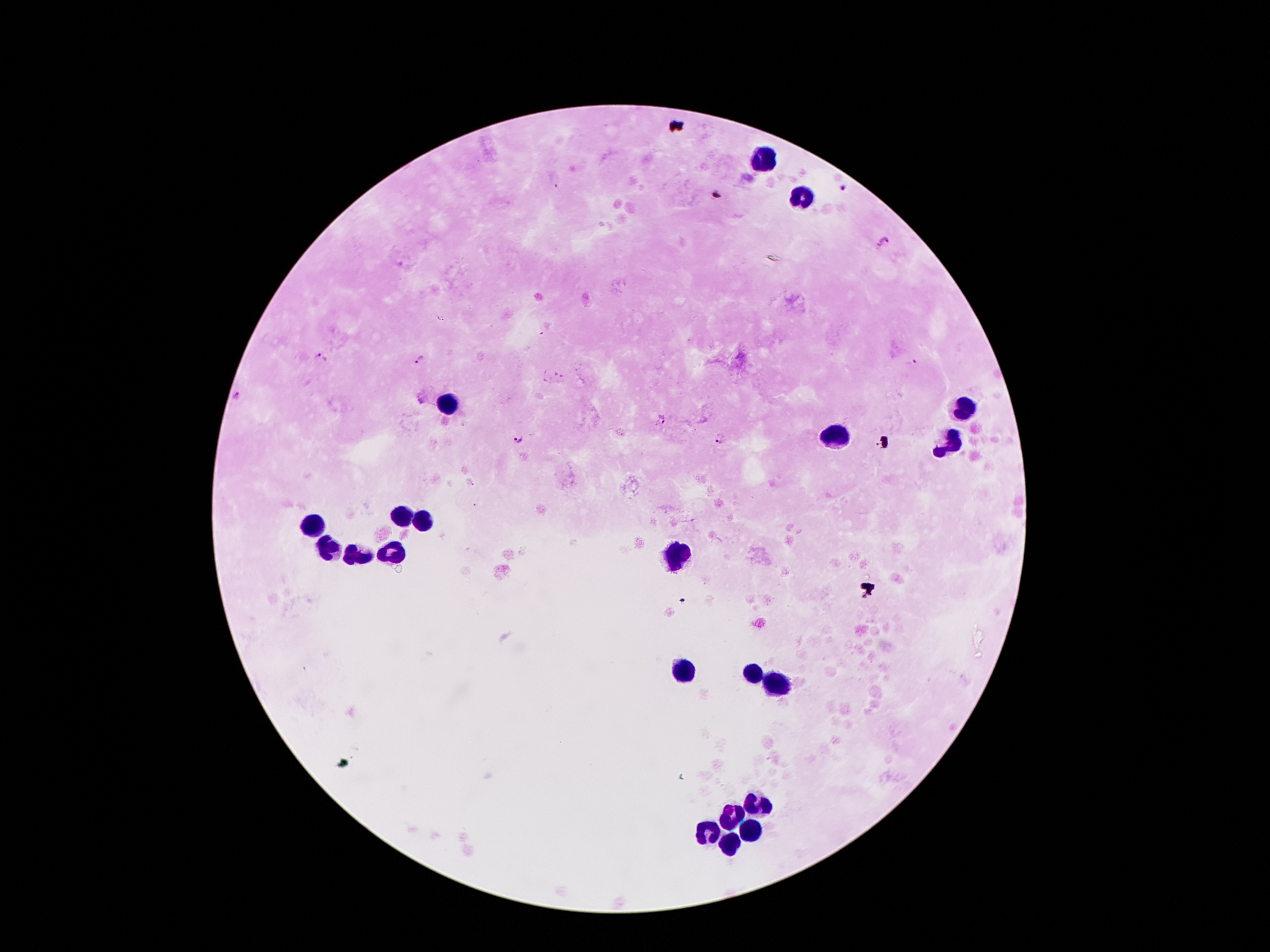

{
  "capture": "smartphone through the microscope eyepiece",
  "image_size": "1270×952 pixels",
  "malaria_parasite_locations": "approximate centers as {x, y} in pixels: {842, 189}, {884, 242}, {321, 357}, {422, 358}, {236, 395}, {660, 421}, {517, 438}, {719, 438}",
  "preparation": "thick blood smear",
  "leukocyte_locations": "approximate centers as {x, y} in pixels: {763, 158}, {802, 196}, {964, 406}, {447, 407}, {839, 438}, {952, 442}, {402, 514}, {424, 522}, {315, 526}, {329, 546}, {395, 552}, {359, 554}, {674, 557}, {686, 670}, {754, 673}, {775, 685}, {758, 804}, {731, 818}, {751, 830}, {711, 832}, {726, 844}",
  "magnification": "100x",
  "patient_malaria_status": "positive for Plasmodium falciparum",
  "field_of_view": "single",
  "stain": "Giemsa"
}